Evaluate for malaria.
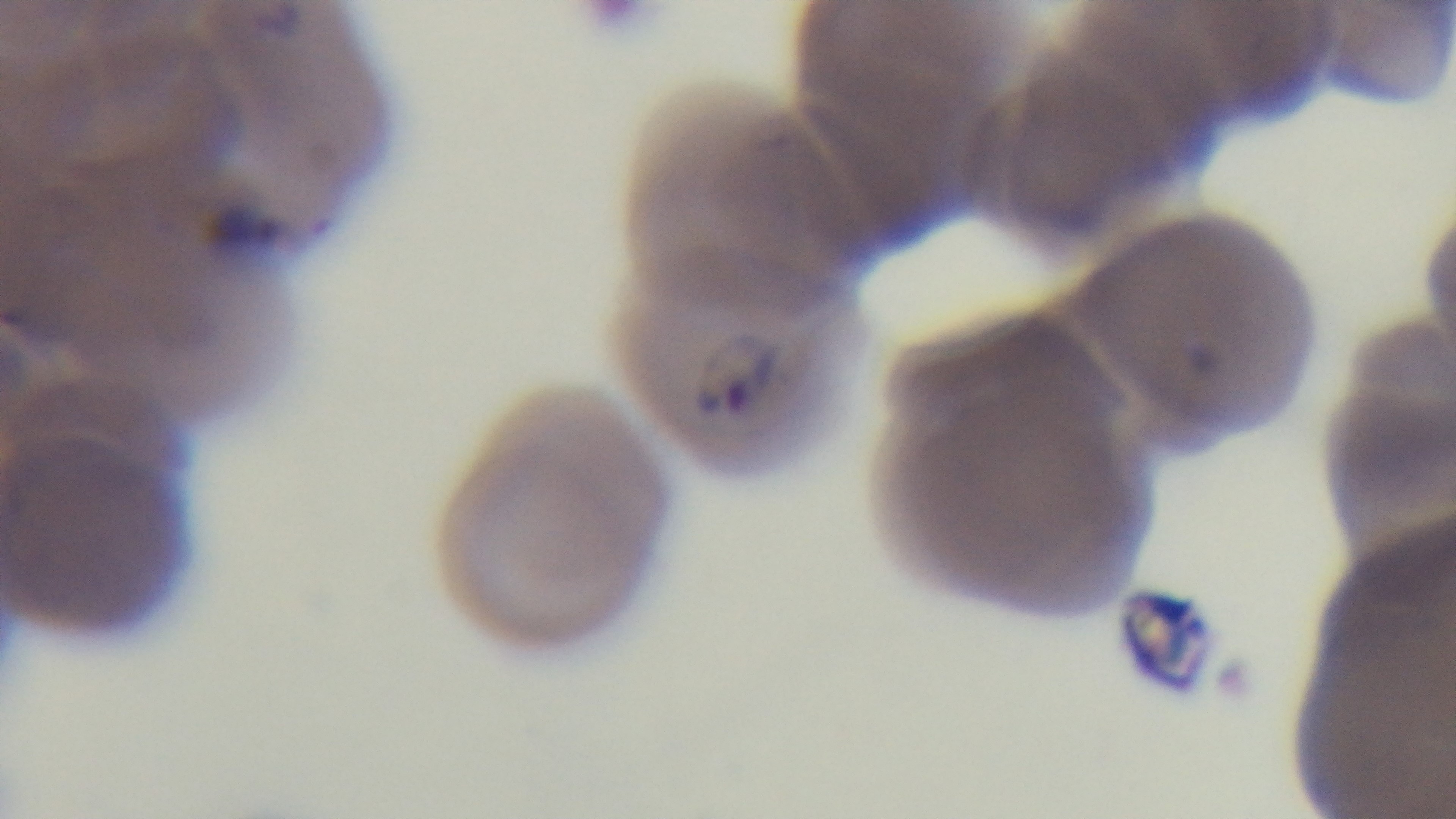

Positive.

Giemsa stain. Preparation: thin smear. Single field of view. Light microscopy. Oil-immersion objective, 100x. Mounted 4K digital camera.